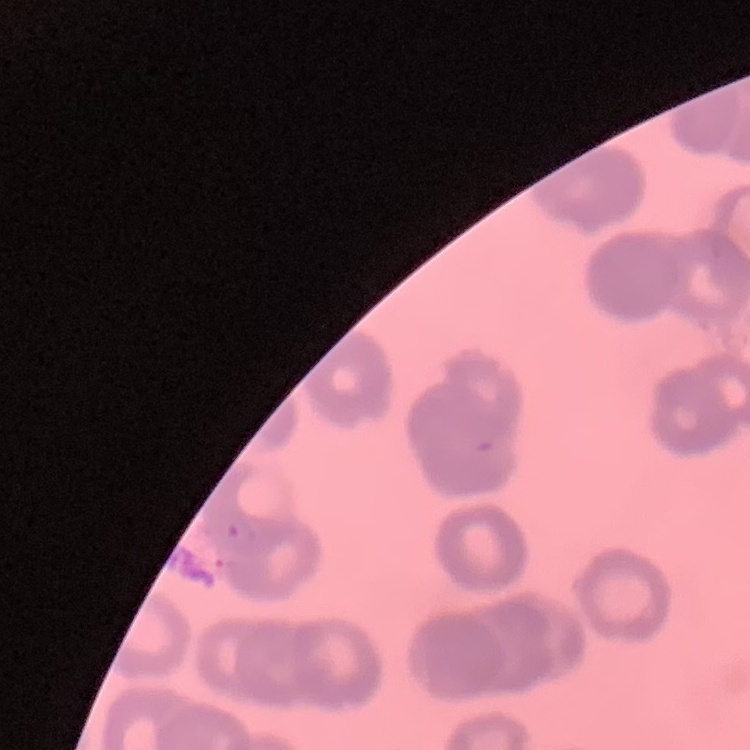
The erythrocytes exhibit rouleaux formation. One tile cut from a larger photomicrograph. Field's or Giemsa stain. Thin blood smear.